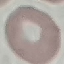
Summary:
  - Result: no malaria parasites detected
  - Capture: smartphone camera at the microscope eyepiece
  - Preparation: thin blood film
  - Image type: automatically extracted cell patch, resized to 64 × 64 pixels
  - Stain: Giemsa